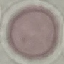

Summary:
  - Malaria status: uninfected
  - Preparation: thin blood smear
  - Stain: Giemsa
  - Image type: cell patch, automatically extracted from a larger field of view and resized to 64 × 64 pixels
  - Capture: smartphone camera at the microscope eyepiece